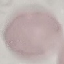

malaria status = uninfected
capture = smartphone camera at the microscope eyepiece
image type = automatically extracted cell patch, resized to 64 × 64 pixels
stain = Giemsa
preparation = thin blood film